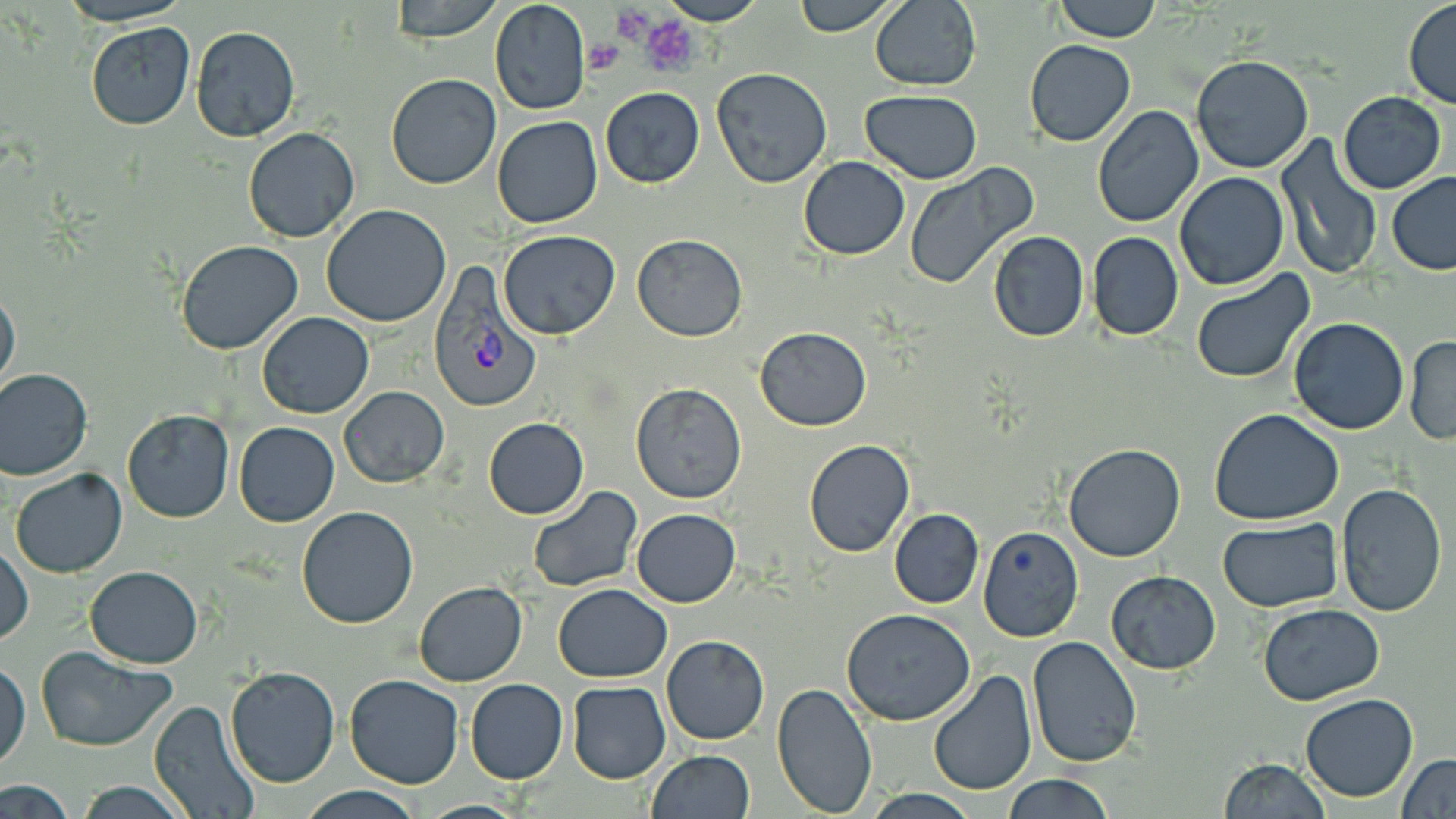

Summary:
  - Coordinate format: approximate bounding boxes as (x1,y1)-(x2,y2) corner pairs in pixels
  - Plasmodium vivax-infected red blood cell locations: (427,262)-(540,413)
  - Uninfected red blood cell locations: (54,0)-(195,27), (388,0)-(507,43), (489,0)-(591,116), (655,0)-(768,25), (790,0)-(901,35), (1054,0)-(1159,42), (1403,1)-(1456,109), (867,2)-(982,90), (84,21)-(196,131), (190,26)-(302,144), (1023,39)-(1136,147), (1190,56)-(1314,174), (711,67)-(832,187), (385,73)-(501,190), (600,87)-(705,188), (859,91)-(983,183), (1337,92)-(1447,193), (1092,105)-(1205,228), (493,115)-(602,229), (242,127)-(360,242), (1275,133)-(1383,280), (799,156)-(910,260), (904,164)-(1037,289), (1387,171)-(1456,274), (1174,173)-(1289,291), (321,204)-(451,327), (498,231)-(620,340), (987,231)-(1090,342), (1086,233)-(1183,341), (631,234)-(747,340), (175,240)-(304,355), (1190,269)-(1314,385), (0,285)-(21,398), (256,312)-(374,420), (1287,317)-(1410,435), (755,327)-(871,429), (1404,336)-(1455,444), (0,368)-(94,480), (630,383)-(747,503), (339,386)-(449,487), (1209,408)-(1344,526), (121,410)-(234,523), (482,417)-(589,520), (234,422)-(339,526), (803,439)-(915,557), (1062,444)-(1186,562), (9,468)-(128,578), (1335,483)-(1447,616), (528,485)-(642,593), (296,506)-(419,629), (632,508)-(742,608), (888,508)-(984,609), (1217,519)-(1343,611), (979,526)-(1083,643), (0,543)-(32,645), (84,565)-(202,666), (1103,571)-(1221,674), (413,580)-(527,686), (553,584)-(673,682), (1258,602)-(1385,706), (840,608)-(977,727), (661,635)-(769,745), (1026,636)-(1142,769), (33,646)-(175,751), (0,659)-(28,770), (224,664)-(340,787), (927,669)-(1037,796), (344,674)-(466,789), (465,679)-(568,784), (772,682)-(877,818), (567,683)-(670,784), (1300,691)-(1418,803), (148,700)-(260,819), (646,750)-(756,819), (1397,753)-(1456,819), (1218,758)-(1332,819), (1003,774)-(1116,819), (0,781)-(79,816), (70,781)-(195,818), (297,788)-(422,819), (857,789)-(985,819), (414,798)-(531,817)
  - Platelet locations: (614,4)-(657,44), (636,14)-(700,76), (583,41)-(623,74)
  - Slide-level diagnosis: Plasmodium vivax
  - Image size: 1456×819 pixels
  - Modality: optical microscopy
  - Field of view: single
  - Preparation: thin blood film
  - Magnification: 1000x
  - Stain: May-Grünwald-Giemsa